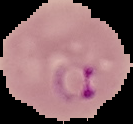
Summary:
  - Preparation: thin blood smear
  - Image type: segmented cell region with the area outside set to black
  - Result: malaria parasites detected
  - Image size: 133×124 pixels